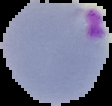
image type = cell region segmented out of the field of view; surrounding area masked to black
preparation = thin blood smear
image size = 112×106 pixels
result = Plasmodium parasites identified